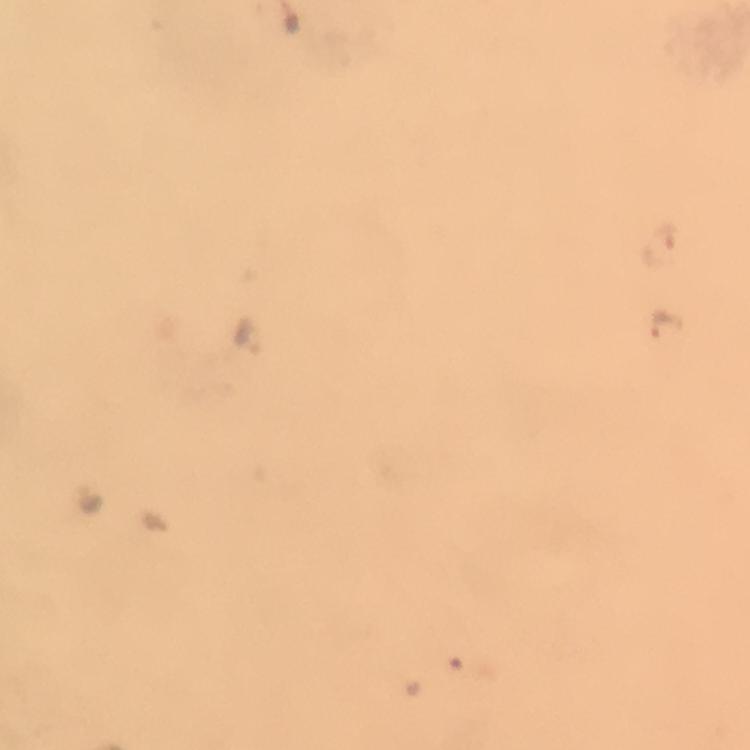

Approximate centers as {x, y} in pixels.
Summary:
  - Plasmodium parasite locations: {669, 323}, {247, 333}
  - Capture: smartphone camera through the microscope
  - Cropped from: one field of view
  - Preparation: thick smear
  - Stain: Giemsa
  - Context: from a diagnostic examination for malaria
  - Immersion oil: used
  - Image size: 750×750 pixels
  - Magnification: 100x